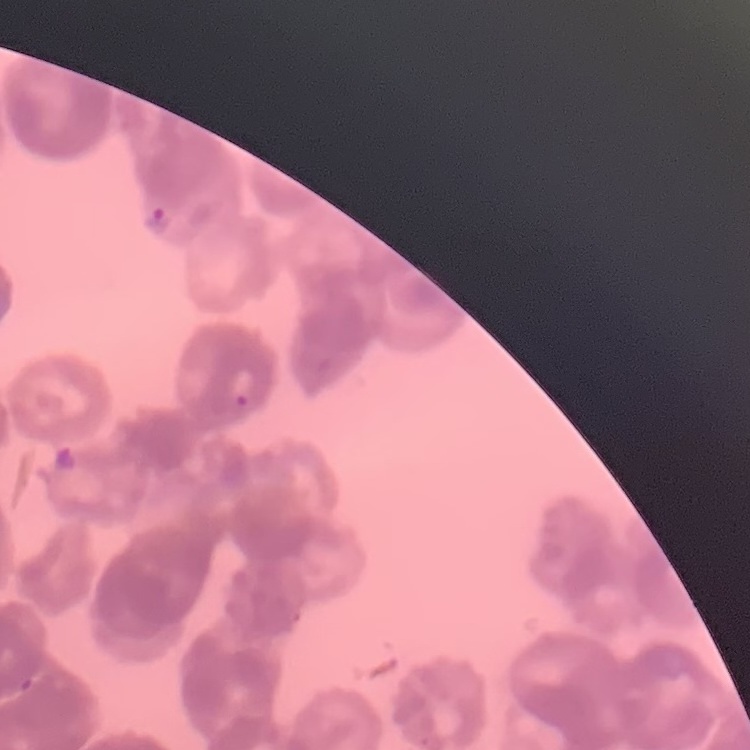
red blood cell morphology = rouleaux formation
stain = Field's or Giemsa
image type = one tile cut from a larger photomicrograph
preparation = thin peripheral smear